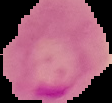

{
  "malaria_status": "parasitized",
  "image_size": "112×103 pixels",
  "preparation": "thin blood film",
  "image_type": "cell region segmented out of the field of view; surrounding area masked to black"
}